Classify this cell by malaria status.
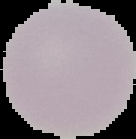
Uninfected.

Summary:
  - Image type: cell region segmented out of the field of view; surrounding area masked to black
  - Image size: 136×139 pixels
  - Preparation: thin blood smear